Identify the parasite.
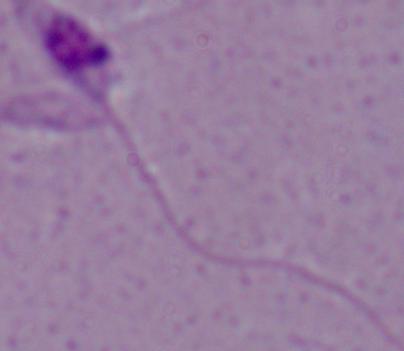
Leishmania.

magnification: 1000x
modality: micrograph